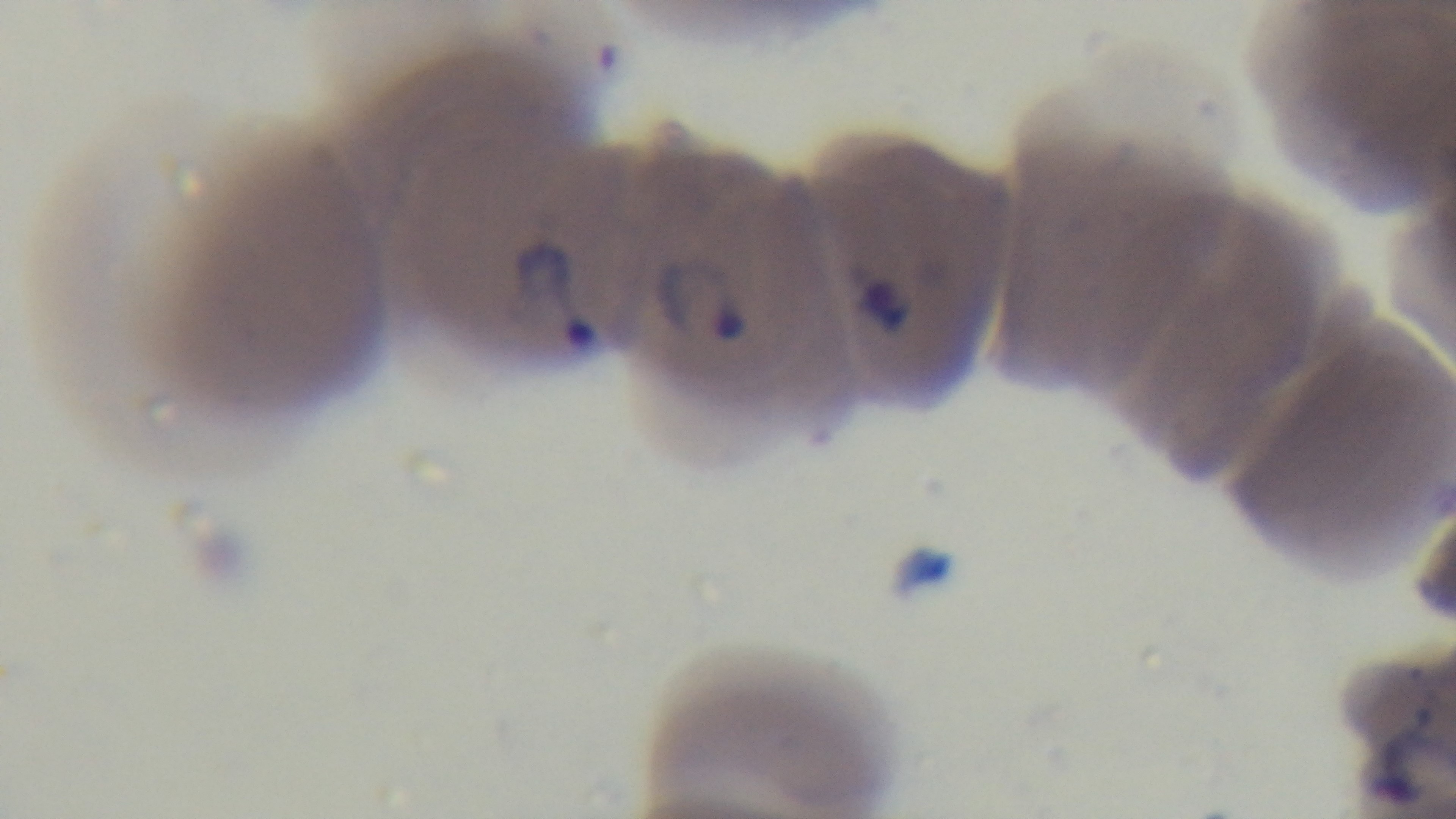

field of view = single
preparation = thin
malaria status = infected
stain = Giemsa
modality = light microscopy
capture = mounted 4K digital camera
objective = 100x oil immersion